Name the cell type shown.
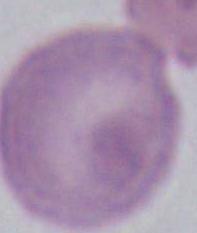

This is an erythrocyte.

modality = photomicrograph
magnification = 1000x